State the blood parasite species.
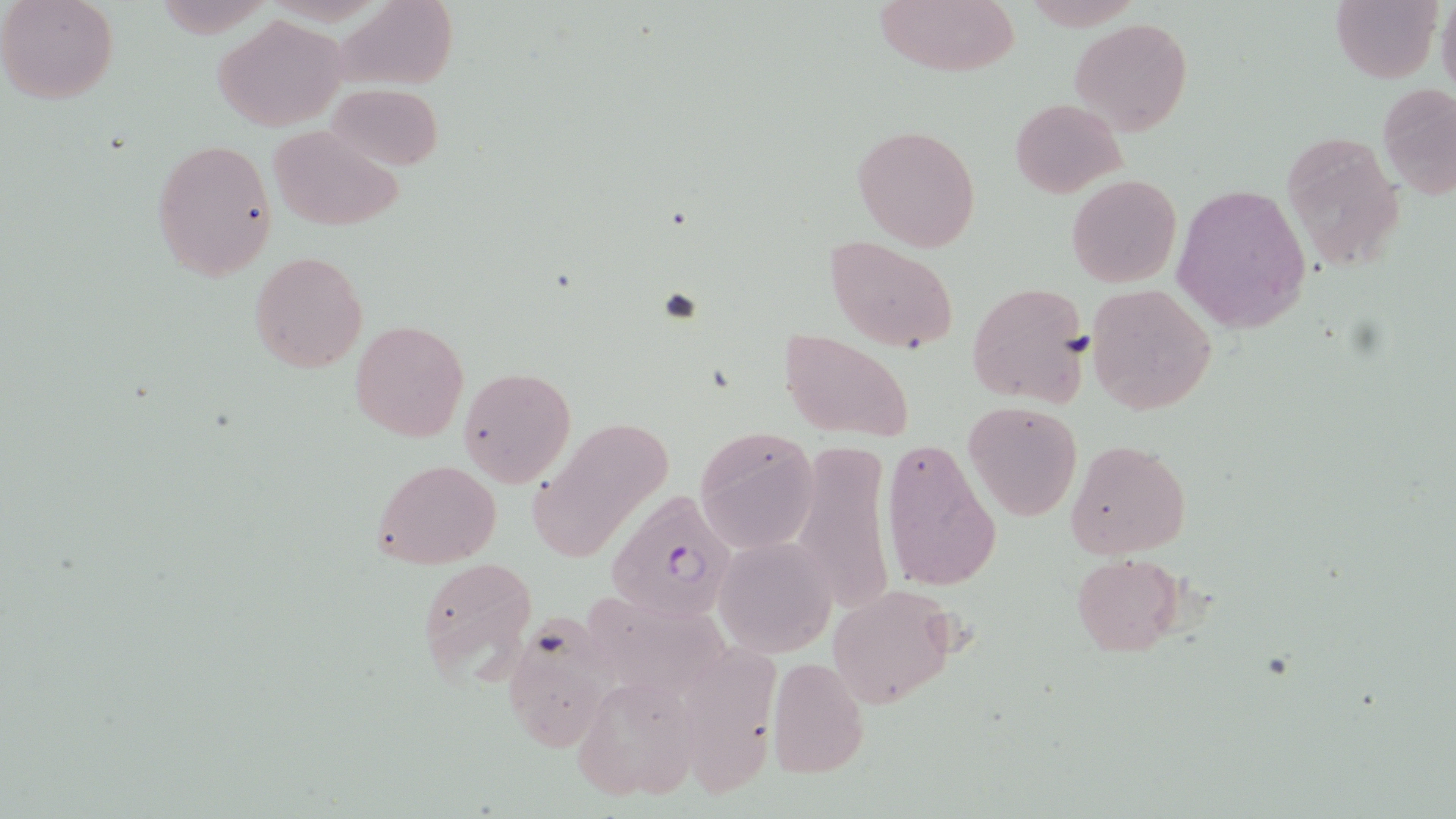
Plasmodium falciparum.

Approximate bounding boxes as [x1, y1, x2, y2] in pixels. Uninfected red blood cell locations: [0, 0, 120, 105], [334, 0, 460, 86], [874, 0, 1020, 77], [1330, 0, 1443, 83], [1437, 0, 1456, 99], [214, 15, 349, 131], [1070, 18, 1192, 137], [326, 82, 444, 171], [1376, 84, 1455, 198], [1010, 98, 1125, 196], [852, 123, 982, 251], [269, 124, 403, 230], [1276, 130, 1405, 273], [149, 138, 278, 281], [1066, 174, 1181, 288], [1171, 182, 1314, 332], [825, 235, 961, 353], [248, 250, 369, 373], [966, 281, 1090, 407], [1086, 283, 1216, 415], [350, 319, 469, 442], [779, 328, 914, 445], [458, 365, 576, 489], [963, 400, 1084, 521], [522, 415, 673, 561], [694, 425, 821, 553], [880, 435, 1004, 593], [1064, 439, 1191, 561], [792, 442, 894, 619], [371, 459, 501, 570], [713, 538, 836, 657], [1069, 554, 1187, 658], [415, 556, 539, 684], [827, 584, 959, 708], [582, 590, 739, 700], [500, 614, 617, 751], [765, 656, 870, 780], [571, 675, 698, 803]. Plasmodium falciparum-infected red blood cell locations: [602, 489, 739, 621]. Optical microscopy. Single field of view. Image is 1456×819 pixels. Captured at 1000x magnification. Thin blood smear. May-Grünwald-Giemsa stain.